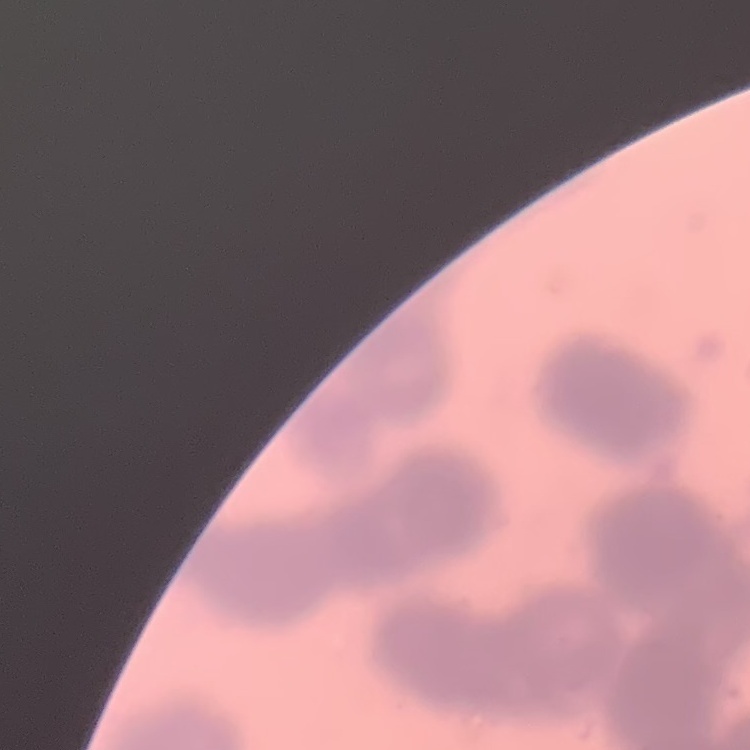
Summary:
  - Red blood cell morphology: rouleaux formation
  - Stain: Field's or Giemsa
  - Preparation: thin peripheral smear
  - Image type: square crop of a larger photomicrograph